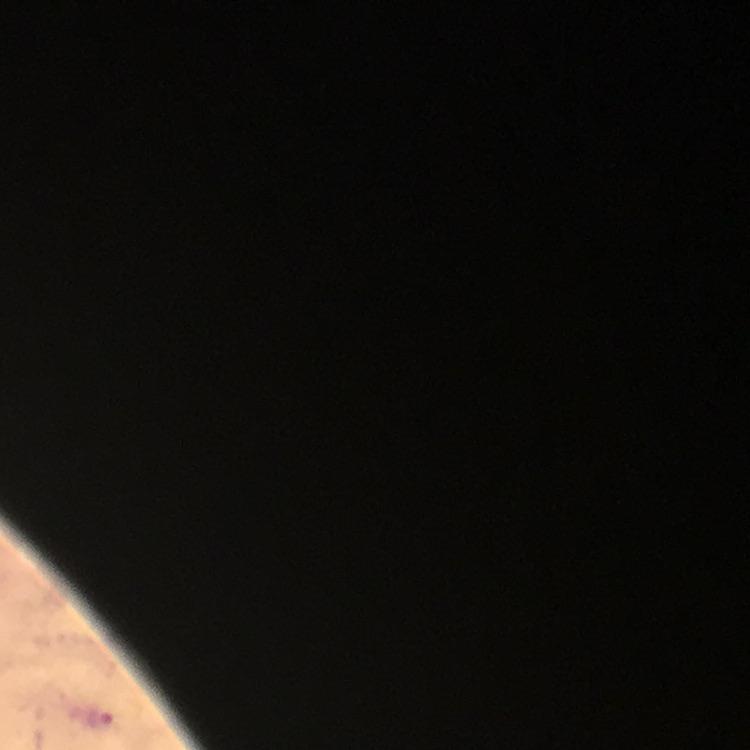

Plasmodium parasite locations = approximate centers as (x, y) in pixels: (101, 722)
magnification = 100x
stain = Giemsa
capture = smartphone camera through the microscope
context = from a diagnostic examination for malaria
immersion oil = applied
image size = 750×750 pixels
cropped from = one field of view
preparation = thick blood film